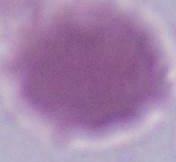 Photomicrograph. An erythrocyte is shown. 1000x magnification.